Report the malaria status of this cell.
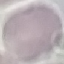

Uninfected.

Photographed with a smartphone camera at the microscope eyepiece. Giemsa stain. Cell patch, automatically extracted from a larger field of view and resized to 64 × 64 pixels. Thin smear of blood.